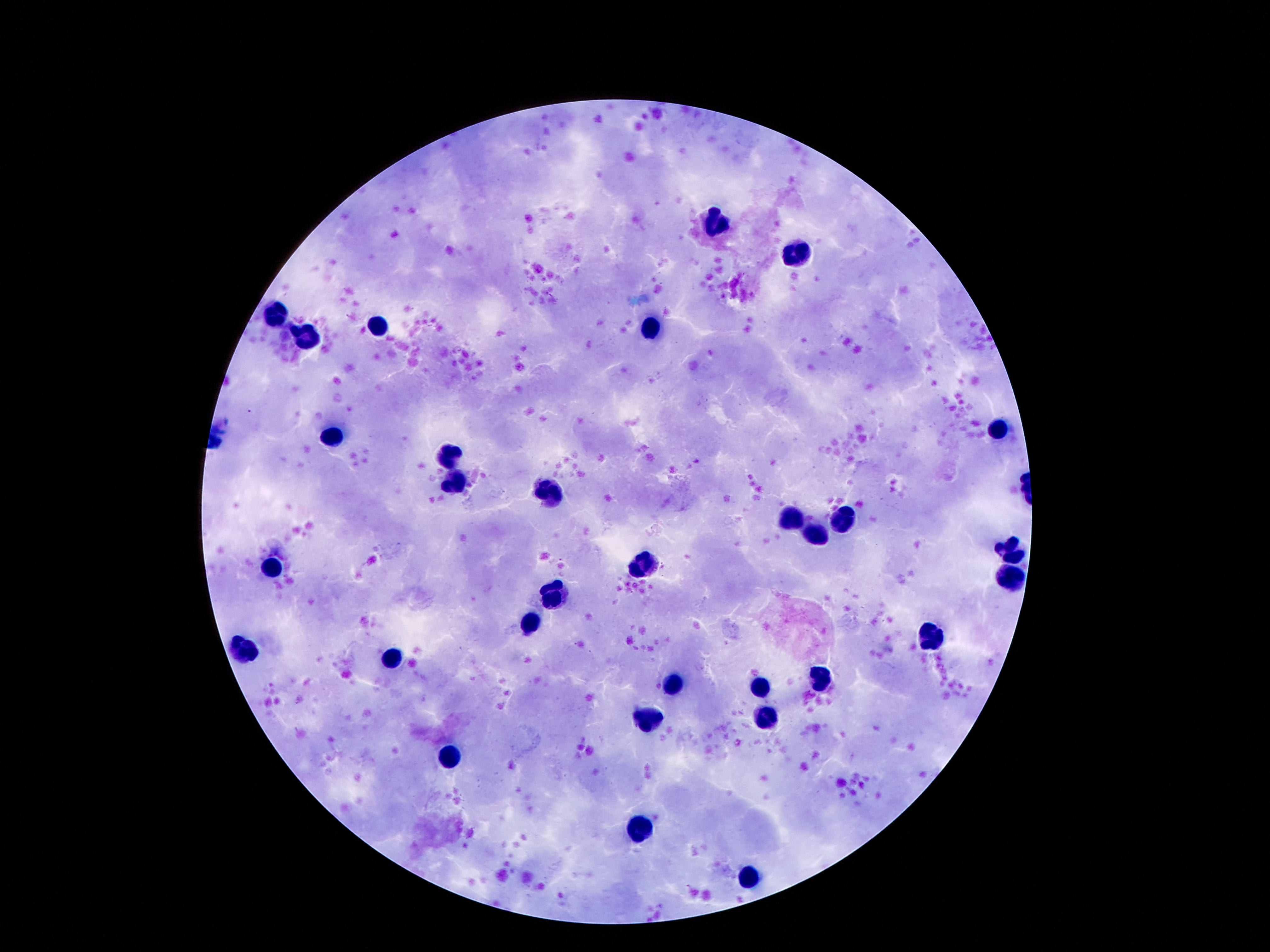

Approximate centers as {x, y} in pixels. Leukocyte locations: {715, 225}, {799, 253}, {279, 313}, {379, 324}, {651, 329}, {306, 339}, {996, 428}, {332, 435}, {445, 457}, {454, 485}, {547, 496}, {845, 514}, {795, 518}, {821, 533}, {1009, 551}, {646, 563}, {271, 569}, {1011, 574}, {558, 596}, {527, 625}, {932, 634}, {242, 647}, {392, 657}, {819, 677}, {671, 684}, {759, 686}, {649, 720}, {764, 721}, {452, 753}, {640, 828}, {746, 876}. 100x magnification. Image is 1270×952 pixels. Thick peripheral-blood smear. Patient malaria status: not infected. Smartphone photograph taken through the microscope eyepiece. One field from this slide. Giemsa-stained preparation.